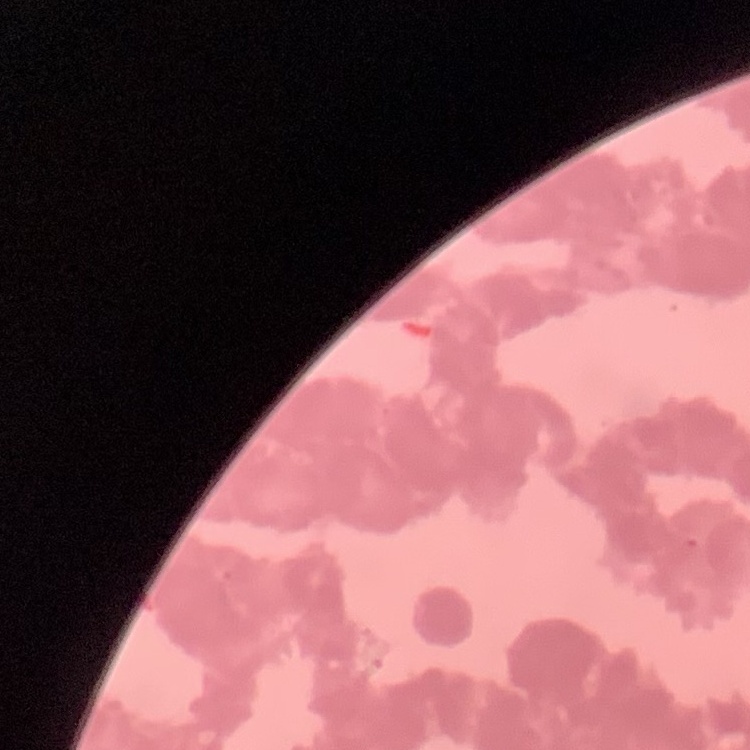

red blood cell morphology = rouleaux formation
stain = Field's or Giemsa
preparation = thin peripheral smear
image type = square crop of a larger photomicrograph